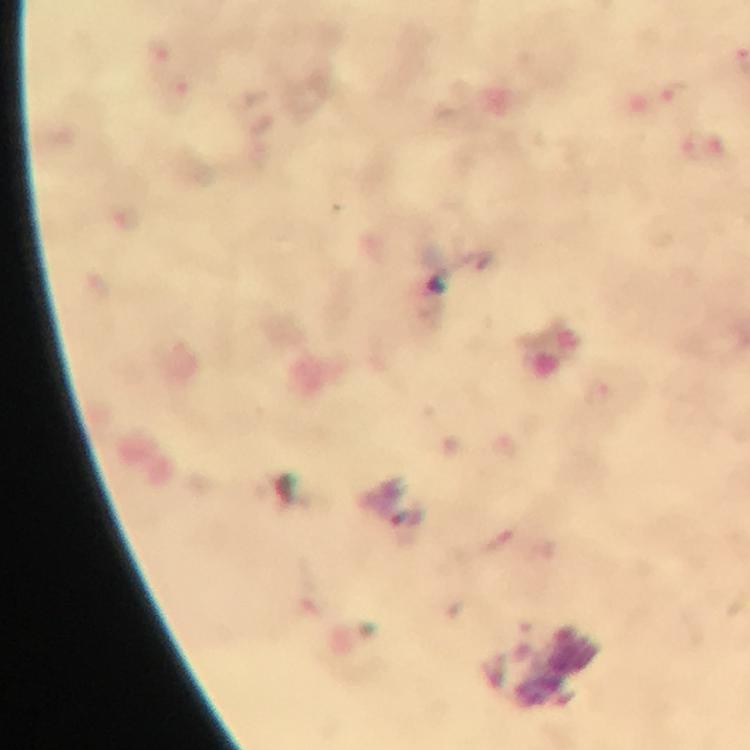
Approximate object centers, in pixels from the top-left corner.
Summary:
  - Malaria parasite locations: (x=673, y=94)
  - Stain: Giemsa
  - Magnification: 100x
  - Preparation: thick blood smear
  - Immersion oil: applied
  - Cropped from: one field of view
  - Context: from a malaria diagnostic workup
  - Image size: 750×750 pixels
  - Capture: smartphone mounted on the microscope